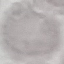

result = negative for malaria parasites
image type = cell patch, automatically extracted from a larger field of view and resized to 64 × 64 pixels
preparation = thin blood film
capture = smartphone through the microscope eyepiece
stain = Giemsa